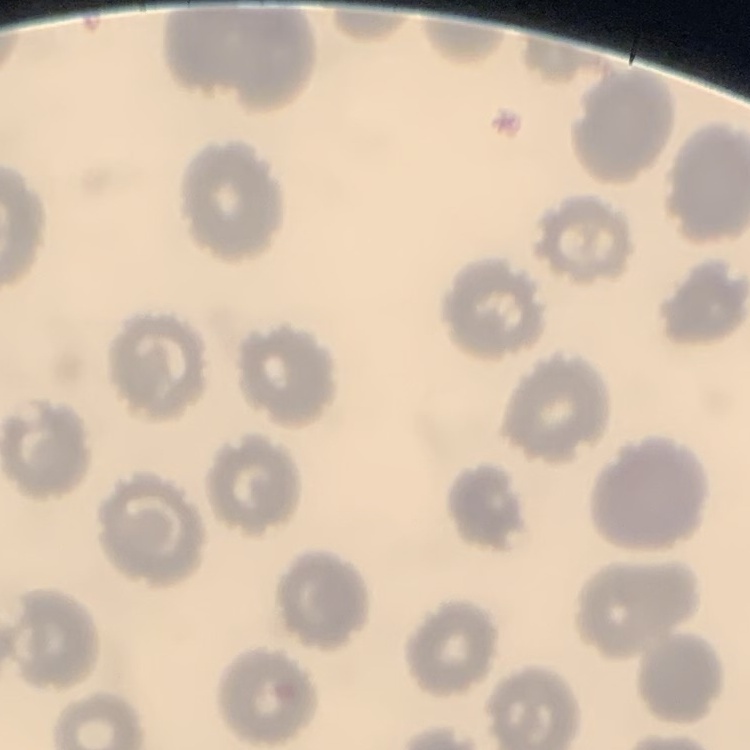

red blood cell morphology = no rouleaux formation
image type = square crop of a larger photomicrograph
preparation = thin peripheral smear
stain = Field's or Giemsa